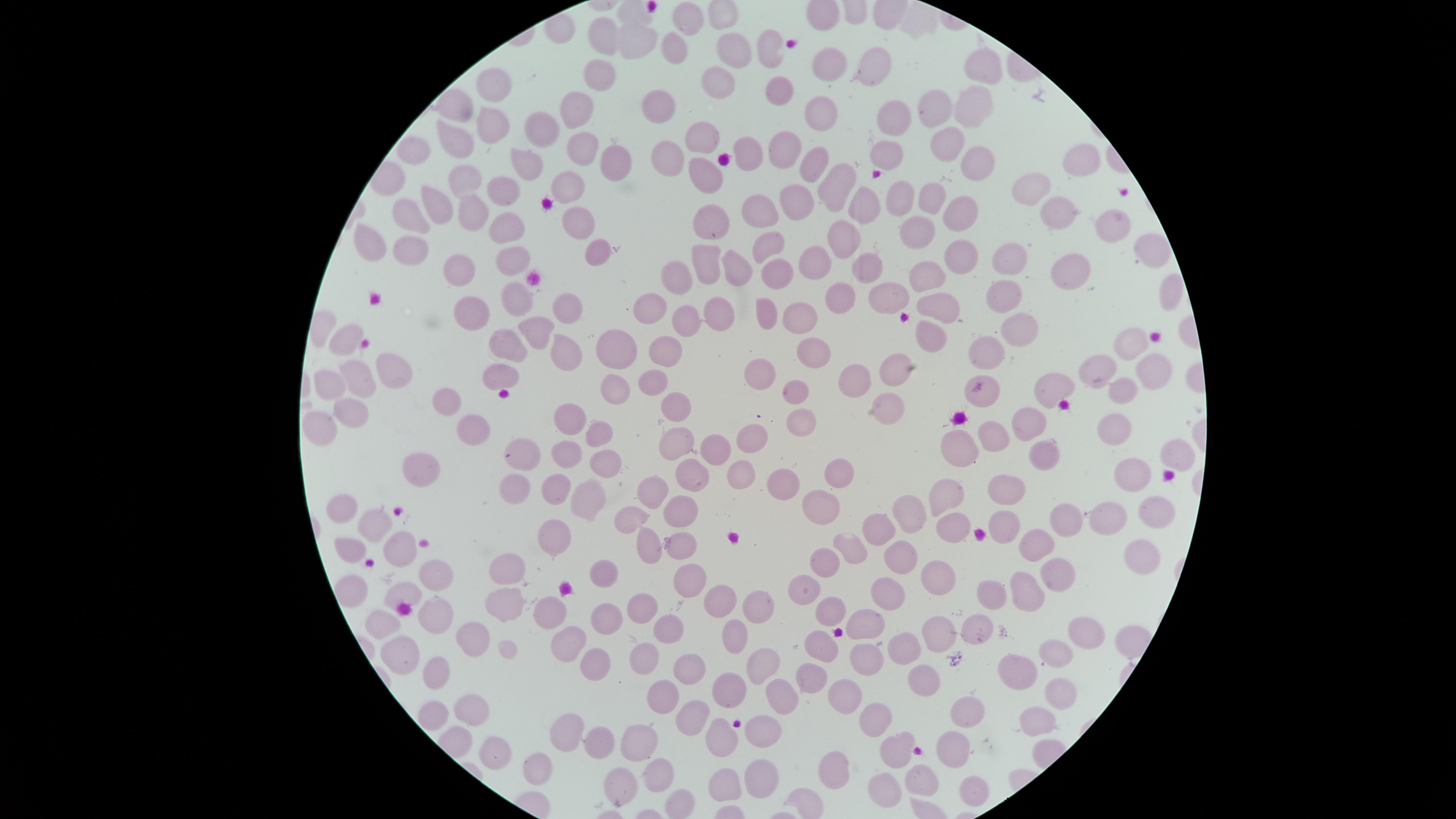
uninfected RBCs = approximate marker points as [x, y] in pixels: [683, 22], [602, 38], [629, 43], [768, 43], [673, 47], [730, 52], [872, 64], [976, 65], [823, 69], [599, 70], [721, 80], [496, 82], [777, 90], [575, 105], [659, 105], [935, 105], [816, 110], [969, 112], [887, 119], [490, 125], [537, 135], [459, 137], [700, 137], [947, 144], [418, 150], [575, 150], [783, 153], [749, 155], [888, 155], [1084, 158], [671, 159], [606, 161], [523, 164], [811, 165], [972, 165], [705, 173], [465, 179], [835, 179], [565, 181], [499, 189], [1028, 193], [895, 200], [936, 200], [800, 202], [437, 208], [863, 208], [471, 209], [406, 212], [711, 212], [1053, 212], [766, 213], [964, 213], [1111, 223], [508, 224], [919, 227], [580, 228], [843, 238], [366, 239], [1144, 245], [769, 246], [404, 250], [598, 251], [515, 255], [959, 257], [1015, 258], [818, 261], [867, 265], [702, 266], [1073, 266], [736, 267], [454, 268], [774, 273], [929, 275], [677, 281], [1001, 291], [882, 294], [835, 296], [510, 298], [939, 305], [569, 309], [763, 312], [653, 314], [806, 315], [475, 318], [680, 319], [719, 323], [1018, 324], [540, 330], [930, 333], [505, 342], [341, 343], [1130, 346], [818, 348], [617, 350], [674, 350], [560, 352], [979, 352], [889, 370], [387, 371], [502, 371], [1095, 373], [1151, 374], [758, 375], [649, 380], [855, 381], [354, 382], [326, 386], [614, 387], [1051, 387], [1122, 392], [791, 394], [980, 396], [446, 399], [680, 410], [567, 411], [879, 411], [348, 414], [1029, 423], [791, 426], [319, 427], [1112, 430], [471, 432], [991, 433], [597, 434], [750, 435], [679, 440], [960, 441], [1045, 450], [1171, 450], [522, 451], [704, 451], [566, 455], [606, 462], [1132, 467], [420, 470], [693, 472], [740, 472], [832, 474], [557, 482], [1001, 483], [517, 484], [780, 486], [654, 492], [953, 492], [586, 497], [819, 506], [1156, 506], [344, 509], [682, 511], [903, 511], [631, 518], [1065, 519], [1108, 519], [953, 522], [375, 523], [1009, 529], [876, 532], [552, 534], [650, 540], [398, 541], [679, 542], [854, 546], [350, 547], [1035, 547], [892, 553], [1137, 553], [829, 563], [1055, 568], [507, 570], [604, 574], [939, 576], [687, 577], [434, 579], [808, 584], [1024, 585], [350, 586], [991, 591], [878, 592], [401, 595], [719, 598], [504, 602], [755, 603], [826, 608], [548, 611], [635, 611], [605, 615], [430, 618], [666, 624], [384, 625], [865, 625], [938, 627], [1085, 630], [973, 632], [737, 635], [565, 637], [471, 639], [909, 643], [818, 646], [1051, 653], [638, 655], [594, 659], [862, 659], [398, 660], [763, 663], [1017, 670], [685, 671], [432, 677], [921, 677], [808, 680], [724, 685], [662, 698], [774, 698], [846, 698], [1053, 703], [472, 707], [961, 713], [689, 714], [426, 715], [873, 722], [1030, 722], [761, 728], [561, 729], [723, 737], [597, 739], [636, 741], [949, 746], [899, 747], [494, 755], [829, 767], [532, 770], [654, 774], [757, 774], [720, 779], [921, 779], [881, 781], [620, 784], [965, 784]
field of view = single
capture = smartphone photograph through the microscope eyepiece
visible region = circular
preparation = thin blood film
image size = 1456×819 pixels
stain = Giemsa
presence = no malaria parasites identified